Locate Plasmodium parasites and leukocytes.
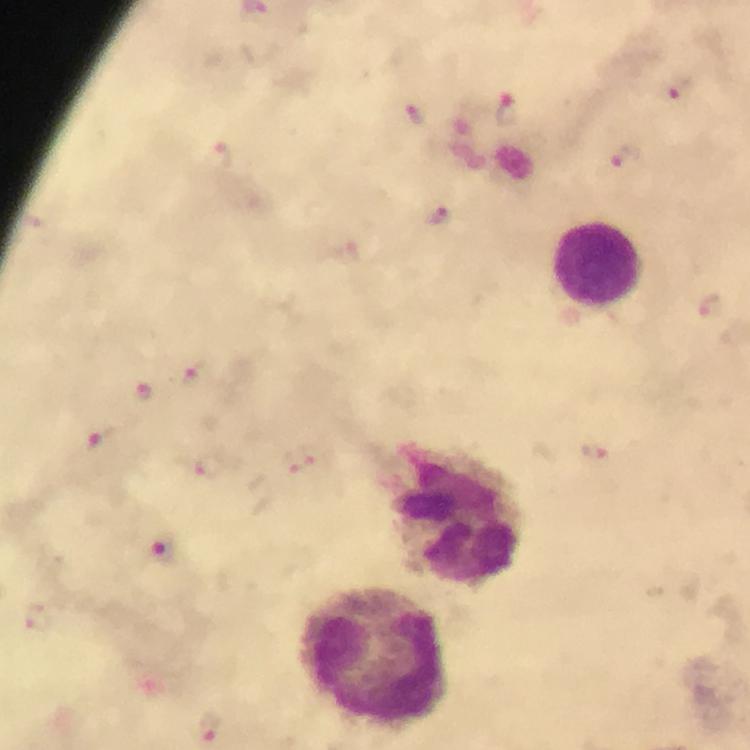

Approximate centers as [x, y] in pixels.
Plasmodium parasites: [679, 89], [507, 111], [414, 114], [625, 155], [217, 156], [439, 218], [196, 372], [145, 391], [102, 439], [595, 451], [309, 461], [210, 466], [159, 549], [38, 617], [210, 729].
Leukocytes: [597, 263], [460, 515], [373, 655].

100x magnification. Immersion oil applied. Giemsa-stained preparation. Thick smear. From a malaria diagnostic workup. A crop from one field of view. Image is 750×750 pixels. Photographed through the microscope with a smartphone camera.